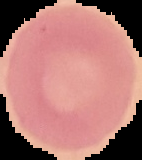
image type = cell region segmented out of the field of view; surrounding area masked to black
preparation = thin blood smear
malaria status = uninfected
image size = 142×160 pixels